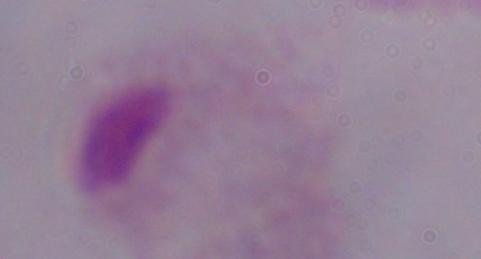

A trichomonad is shown. 1000x magnification. Micrograph.